Describe the morphology of the red blood cells.
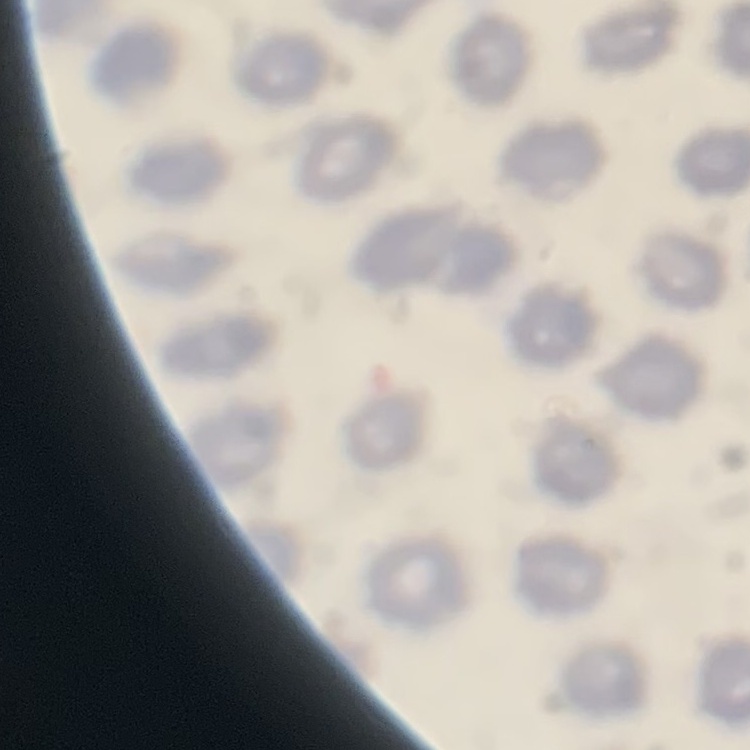
No rouleaux formation.

Summary:
  - Preparation: thin blood smear
  - Stain: Field's or Giemsa
  - Image type: one tile cut from a larger photomicrograph